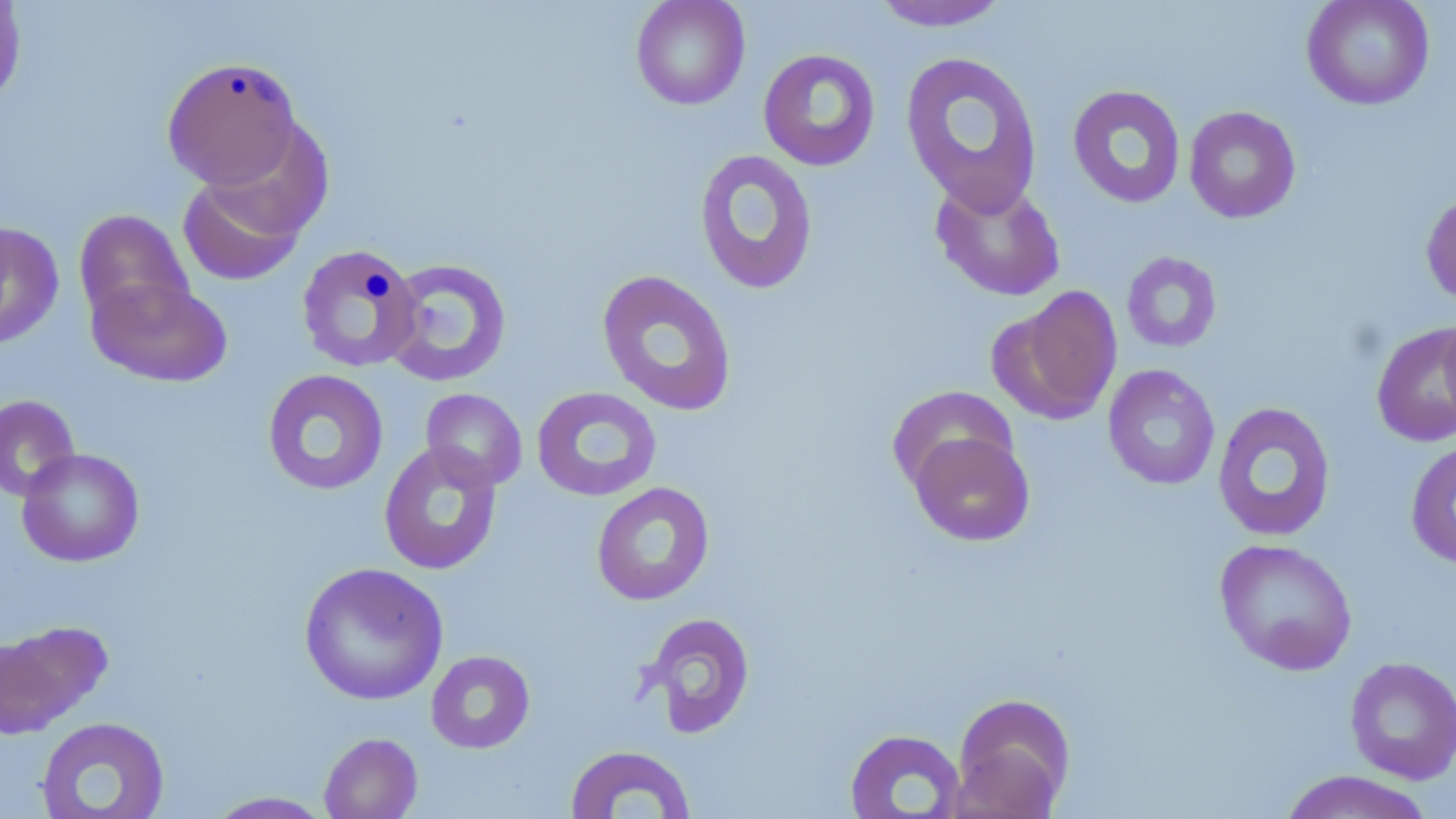

Approximate bounding boxes as (x1, y1, x2, y2) in pixels. Uninfected red blood cell locations: (630, 0, 750, 110), (1301, 0, 1435, 111), (0, 1, 27, 106), (868, 1, 1012, 32), (757, 48, 881, 171), (900, 51, 1044, 213), (162, 57, 304, 191), (1067, 84, 1186, 208), (1184, 106, 1302, 224), (205, 118, 334, 241), (693, 149, 820, 295), (177, 170, 307, 286), (930, 176, 1066, 301), (1420, 191, 1456, 309), (73, 209, 195, 331), (0, 221, 64, 349), (291, 245, 417, 376), (1121, 251, 1222, 353), (383, 257, 512, 388), (596, 269, 738, 416), (88, 274, 233, 388), (997, 285, 1123, 423), (1438, 309, 1456, 429), (1371, 321, 1456, 448), (1103, 364, 1221, 491), (262, 369, 389, 496), (887, 385, 1019, 496), (531, 386, 662, 502), (420, 388, 528, 491), (0, 394, 80, 502), (1212, 401, 1336, 542), (908, 430, 1036, 547), (1405, 439, 1456, 570), (378, 441, 503, 575), (16, 447, 145, 567), (592, 482, 714, 606), (1213, 538, 1358, 676), (298, 562, 449, 706), (639, 612, 756, 739), (0, 621, 110, 737), (426, 650, 535, 754), (1344, 655, 1456, 784), (950, 693, 1076, 817), (35, 716, 170, 818), (844, 728, 967, 818), (319, 732, 423, 819), (564, 744, 696, 818), (1277, 769, 1437, 819), (204, 791, 337, 818). Slide-level diagnosis: negative for blood parasites. Image is 1456×819 pixels. May-Grünwald-Giemsa stain. Single field of view. 1000x magnification. Thin blood smear. Optical microscopy.